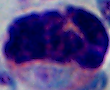 1000x magnification. A leukocyte is shown. Micrograph.